State which parasite is depicted.
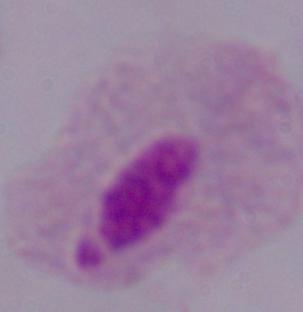
This is a trichomonad.

Summary:
  - Magnification: 1000x
  - Modality: micrograph